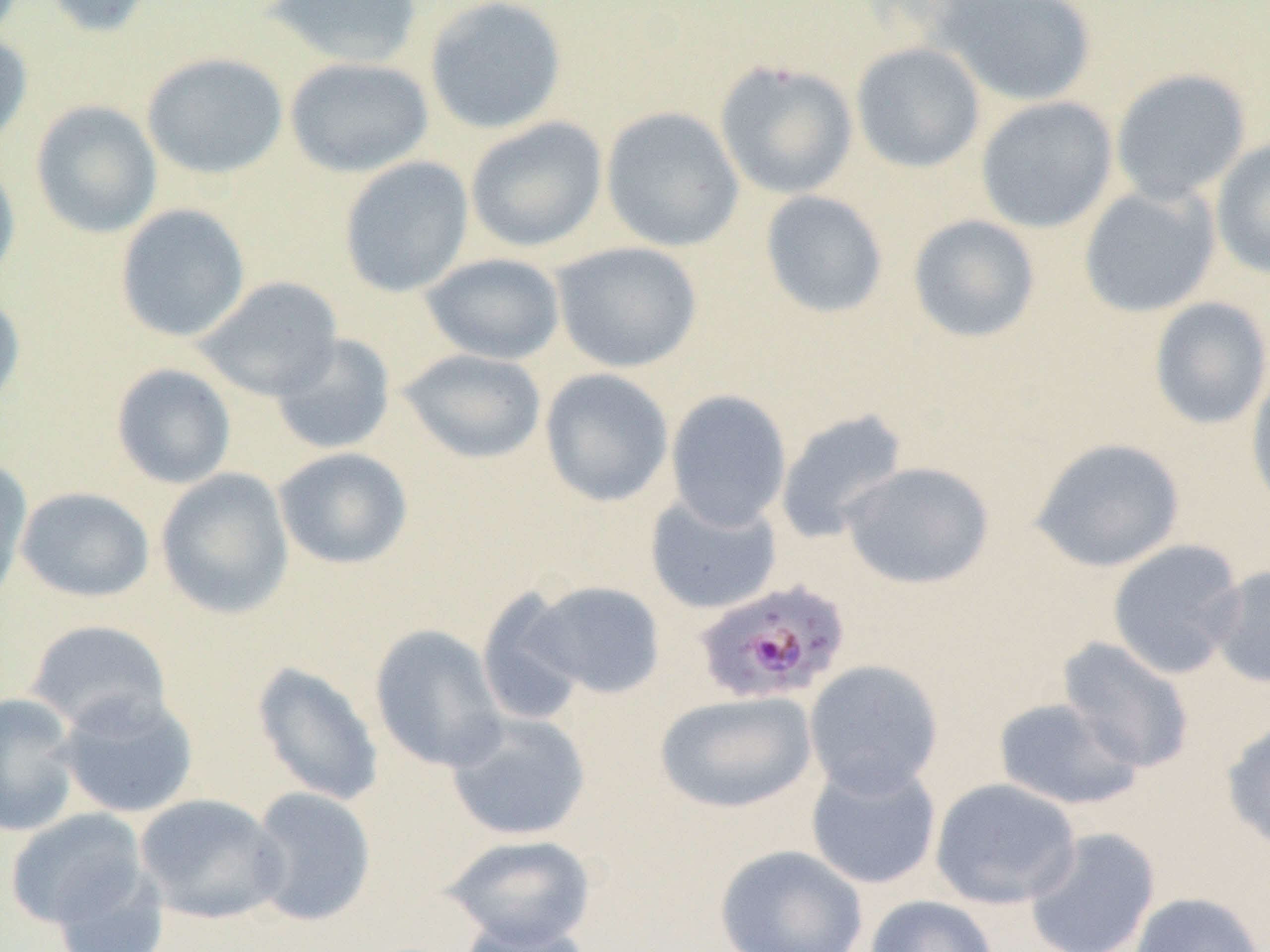
slide-level diagnosis = Plasmodium falciparum
field of view = one of a larger specimen
image size = 1270×952 pixels
Plasmodium falciparum-infected red blood cell locations = approximate bounding boxes as (x1, y1, x2, y2) in pixels: (692, 580, 850, 706)
magnification = 1000x
uninfected red blood cell locations = approximate bounding boxes as (x1, y1, x2, y2) in pixels: (40, 0, 156, 38), (265, 0, 423, 68), (424, 0, 568, 135), (930, 0, 1097, 107), (0, 30, 33, 151), (851, 42, 986, 173), (141, 52, 288, 180), (284, 56, 433, 178), (715, 60, 859, 200), (1109, 68, 1252, 205), (975, 96, 1118, 234), (30, 100, 162, 238), (601, 106, 744, 252), (465, 117, 607, 253), (1210, 137, 1270, 280), (0, 155, 21, 286), (339, 156, 474, 297), (1078, 183, 1221, 318), (759, 190, 889, 319), (114, 203, 251, 342), (907, 214, 1041, 343), (551, 241, 703, 373), (420, 253, 566, 365), (194, 275, 343, 401), (0, 291, 26, 410), (1149, 296, 1270, 430), (270, 333, 396, 455), (398, 348, 547, 464), (111, 363, 236, 489), (1246, 364, 1270, 516), (539, 368, 674, 507), (665, 389, 792, 531), (774, 409, 909, 545), (1029, 436, 1185, 572), (273, 447, 414, 570), (0, 456, 33, 607), (840, 461, 994, 590), (156, 468, 294, 619), (16, 486, 155, 602), (645, 492, 783, 615), (1106, 539, 1245, 679), (1207, 564, 1270, 689), (523, 579, 666, 701), (474, 588, 591, 726), (24, 619, 173, 735), (369, 624, 508, 773), (1057, 637, 1195, 773), (804, 660, 944, 798), (251, 661, 384, 806), (55, 690, 199, 820), (654, 690, 817, 814), (0, 692, 82, 837), (993, 697, 1144, 811), (444, 710, 592, 841), (1221, 715, 1270, 854), (805, 760, 942, 889), (930, 777, 1081, 910), (247, 786, 377, 926), (134, 793, 289, 924), (4, 809, 151, 933), (1024, 827, 1161, 952), (440, 833, 596, 949), (713, 843, 868, 952), (1129, 891, 1265, 952), (864, 894, 1000, 952), (458, 918, 594, 952)
modality = light microscopy
preparation = thin blood smear